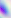
Captured at 400x magnification. Toxoplasma gondii is seen. Photomicrograph.